Assess the morphology of the erythrocytes.
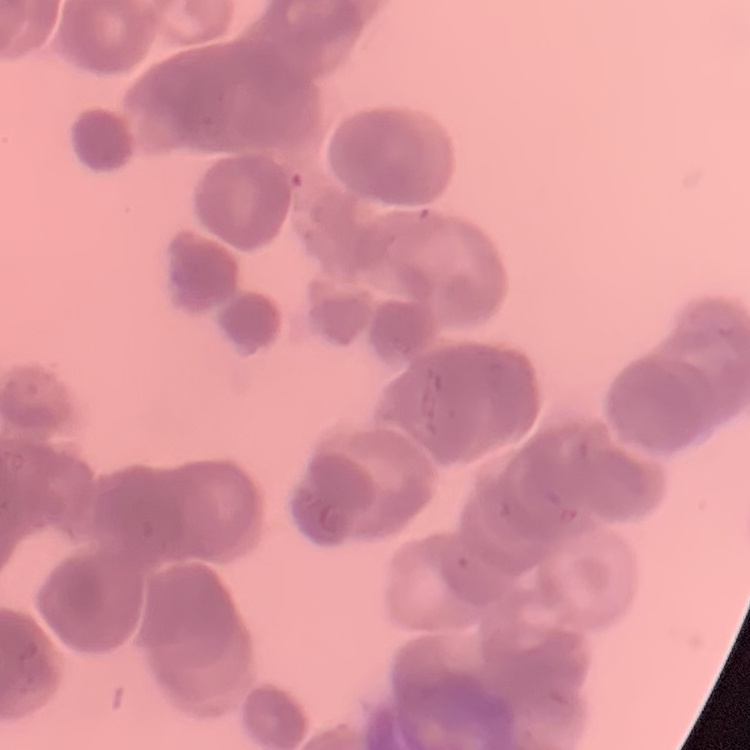
Rouleaux formation.

Summary:
  - Image type: one tile cut from a larger photomicrograph
  - Stain: Field's or Giemsa
  - Preparation: thin blood film